Identify the blood parasite species.
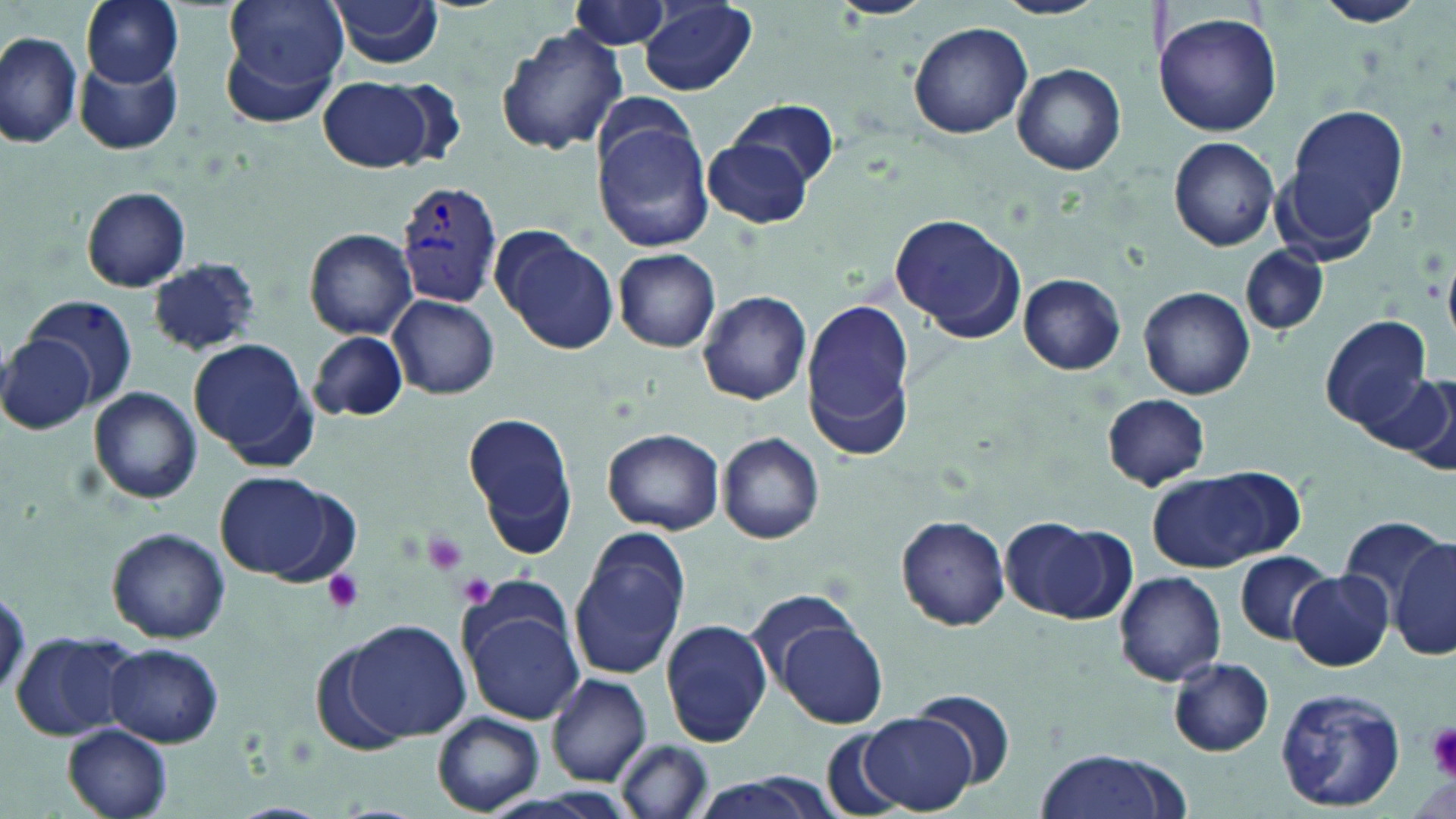
Plasmodium vivax.

{
  "uninfected_red_blood_cell_locations": "approximate bounding boxes as (x1,y1)-(x2,y2) corner pairs in pixels: (83,0)-(184,88), (225,0)-(351,92), (328,0)-(446,69), (826,0)-(937,20), (989,0)-(1109,19), (1312,0)-(1428,28), (638,1)-(757,94), (569,2)-(675,51), (1151,10)-(1281,138), (908,22)-(1034,139), (495,25)-(627,157), (0,32)-(83,151), (218,36)-(341,130), (76,55)-(183,155), (1012,63)-(1126,175), (318,77)-(439,173), (733,99)-(839,190), (1282,103)-(1409,243), (593,118)-(715,253), (1170,137)-(1279,250), (703,140)-(812,228), (81,186)-(192,292), (890,214)-(1026,342), (491,225)-(619,355), (304,228)-(418,340), (1242,245)-(1330,336), (613,248)-(722,352), (146,258)-(260,357), (1018,274)-(1125,375), (1138,286)-(1255,399), (697,289)-(813,405), (26,295)-(141,407), (388,295)-(499,399), (801,297)-(917,457), (1319,315)-(1430,429), (308,318)-(496,413), (310,330)-(410,422), (0,331)-(95,436), (189,339)-(314,461), (1368,369)-(1455,465), (87,387)-(203,502), (1101,394)-(1211,491), (464,412)-(579,550), (602,427)-(725,533), (716,432)-(826,544), (1148,470)-(1293,572), (215,471)-(338,579), (896,514)-(1009,630), (1341,515)-(1447,617), (1002,517)-(1119,620), (106,526)-(232,644), (568,528)-(692,679), (1391,536)-(1456,663), (1234,550)-(1333,644), (1289,570)-(1392,671), (1114,571)-(1227,685), (748,591)-(866,689), (460,602)-(584,724), (772,611)-(889,728), (345,618)-(470,742), (661,619)-(773,749), (11,629)-(135,741), (105,643)-(224,746), (1169,657)-(1273,757), (546,673)-(651,786), (1271,685)-(1408,811), (911,690)-(1015,790), (432,711)-(543,815), (859,712)-(977,812), (63,723)-(172,819), (822,725)-(906,817), (616,737)-(710,818), (1037,749)-(1175,819), (674,775)-(847,819)",
  "field_of_view": "single",
  "preparation": "thin blood smear",
  "magnification": "1000x",
  "image_size": "1456×819 pixels",
  "plasmodium_vivax_infected_red_blood_cell_locations": "approximate bounding boxes as (x1,y1)-(x2,y2) corner pairs in pixels: (397,179)-(505,308)",
  "platelet_locations": "approximate bounding boxes as (x1,y1)-(x2,y2) corner pairs in pixels: (420,530)-(470,577), (321,570)-(366,614), (457,573)-(498,609), (1424,721)-(1456,777)",
  "stain": "May-Grünwald-Giemsa",
  "modality": "light microscopy"
}